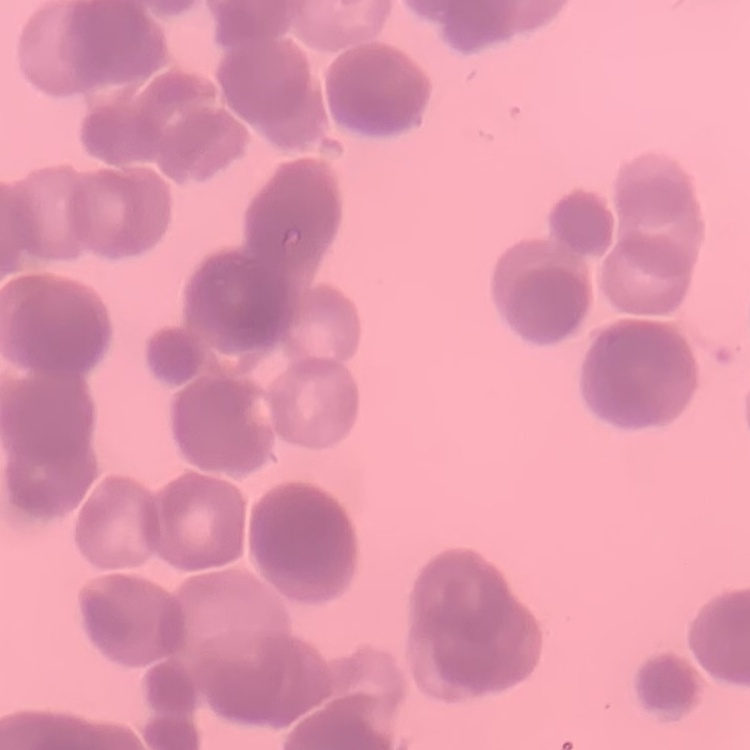

{
  "erythrocyte_morphology": "rouleaux formation",
  "image_type": "one tile cut from a larger photomicrograph",
  "stain": "Field's or Giemsa",
  "preparation": "thin blood film"
}